Assess this cell for malaria.
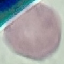
It is uninfected.

preparation = thin blood smear
image type = cell patch, automatically extracted from a larger field of view and resized to 64 × 64 pixels
capture = smartphone through the microscope eyepiece
stain = Giemsa